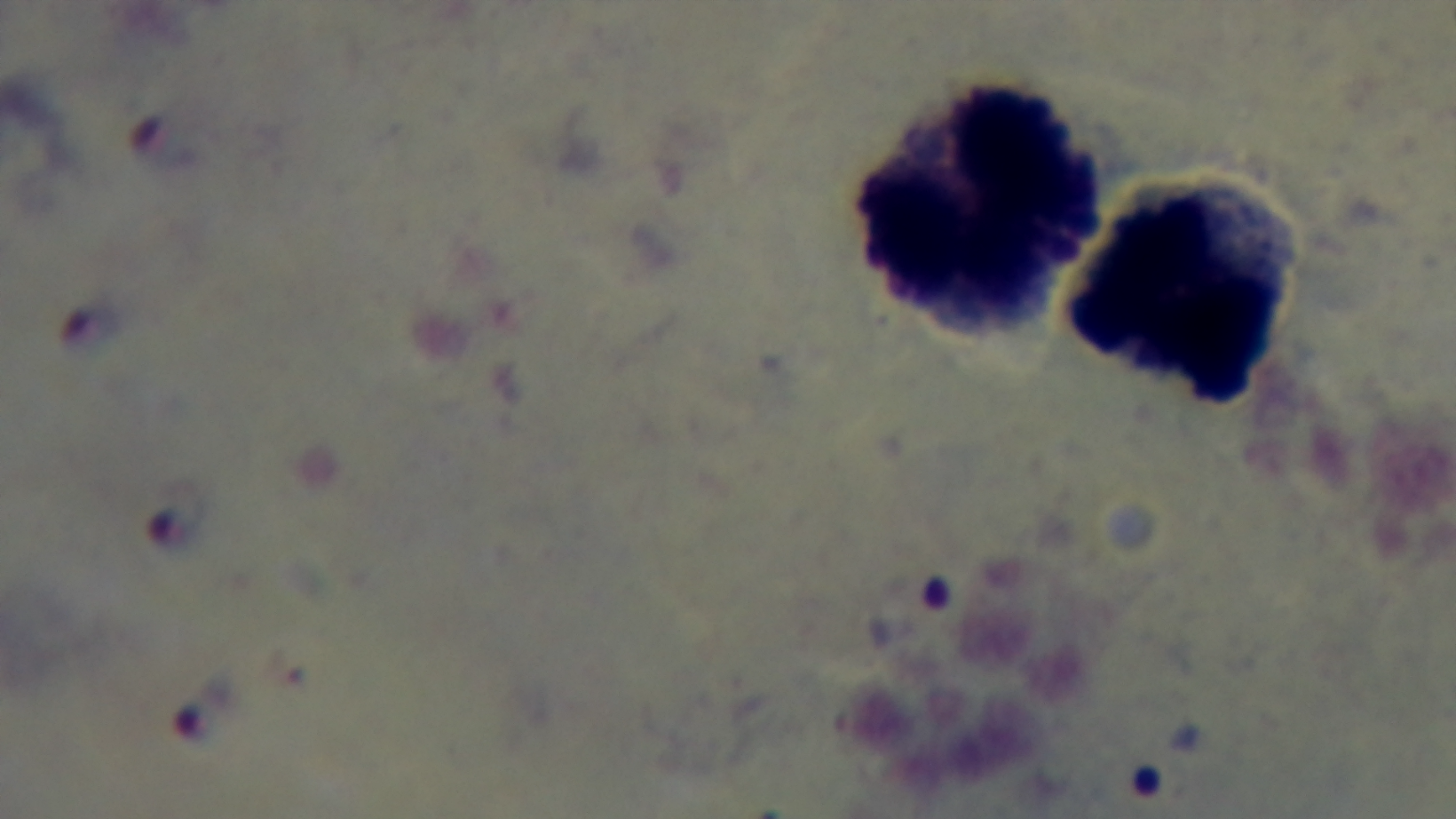

Preparation: thick blood film. Single field of view. Giemsa stain. Malaria status: infected. 100x oil-immersion objective. Mounted 4K digital camera. Photomicrograph.